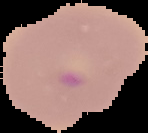
image size = 148×133 pixels
malaria status = parasitized
preparation = thin blood film
image type = segmented cell region with the area outside set to black